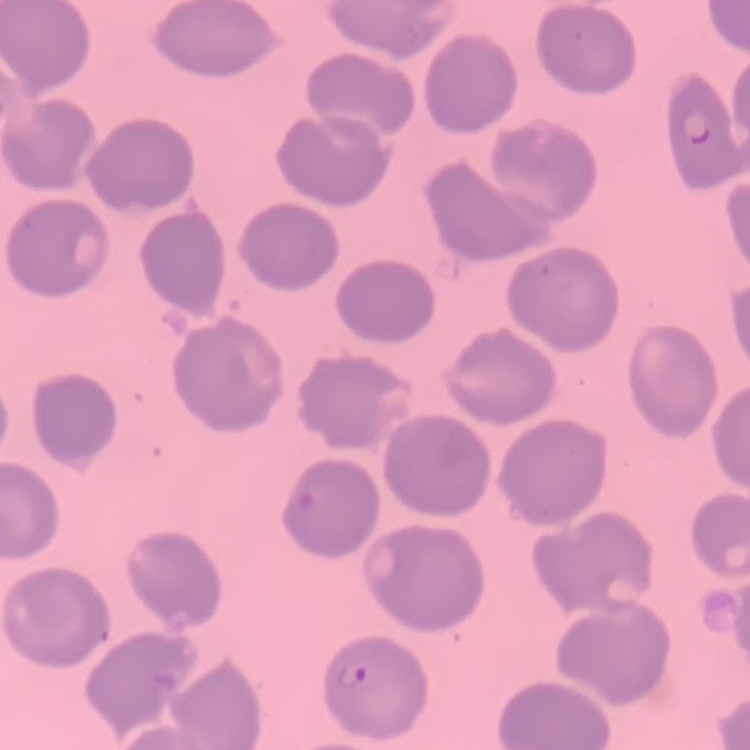

The erythrocytes exhibit no rouleaux formation. Field's or Giemsa stain. One tile cut from a larger photomicrograph. Thin blood film.